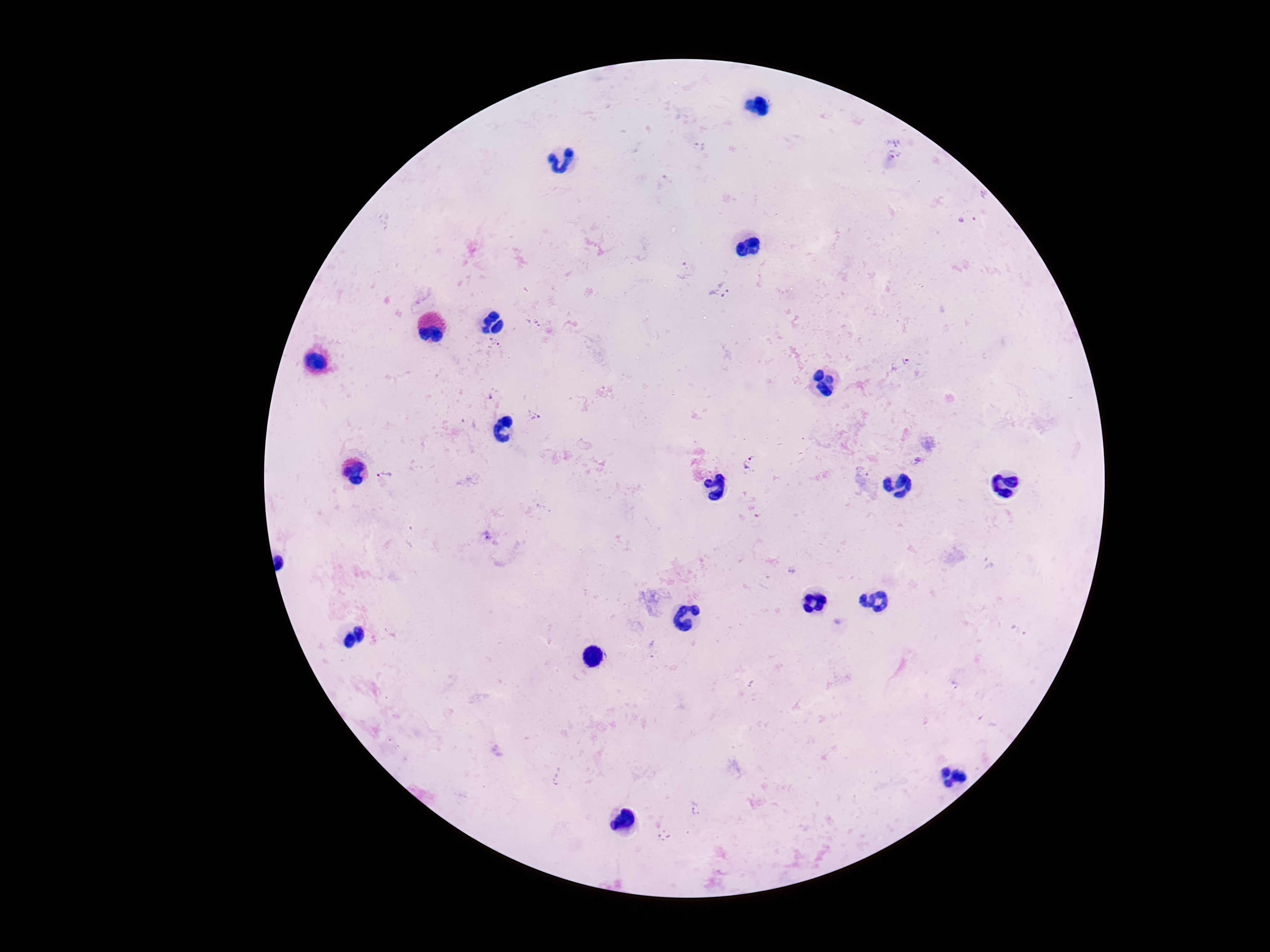
Approximate object centers, in pixels from the top-left corner.
Summary:
  - Plasmodium parasite locations: (x=686, y=271), (x=719, y=291), (x=534, y=325), (x=493, y=343), (x=907, y=361), (x=535, y=416), (x=749, y=462), (x=864, y=471), (x=383, y=475), (x=410, y=537), (x=792, y=570), (x=665, y=836)
  - Magnification: 100x
  - Image size: 1270×952 pixels
  - Field of view: single
  - Patient malaria status: infected
  - Stain: Giemsa
  - Preparation: thick blood film
  - Capture: smartphone camera through the microscope eyepiece